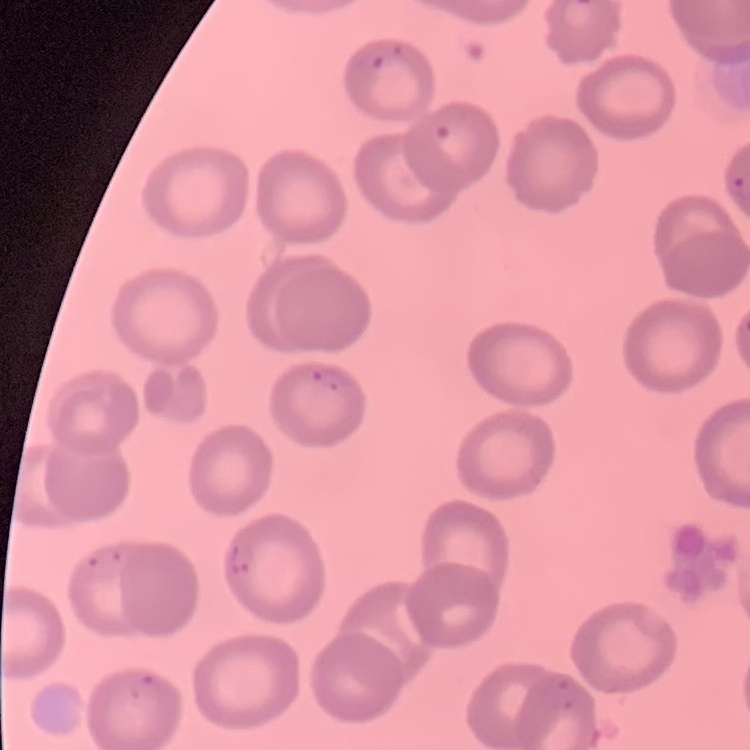
erythrocyte morphology = no rouleaux formation
preparation = thin blood smear
image type = one tile cut from a larger photomicrograph
stain = Field's or Giemsa